Assess this cell for malaria.
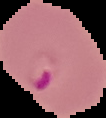
Parasitized.

Image is 106×118 pixels. Segmented cell region on a black background. From a thin blood film.